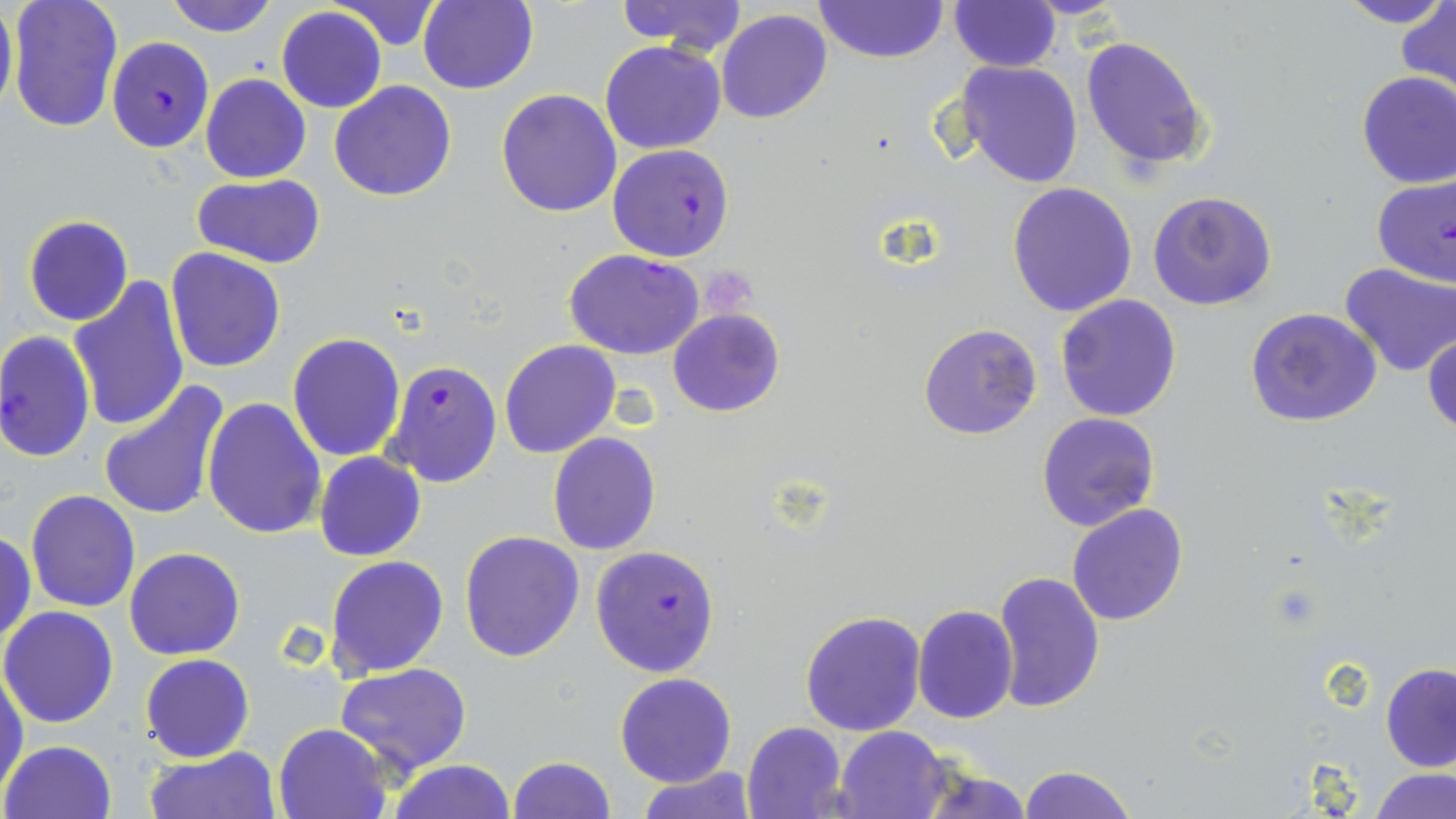
slide-level diagnosis = Plasmodium falciparum
magnification = 1000x
image size = 1456×819 pixels
field of view = single
preparation = thin blood smear
platelet locations = approximate bounding boxes as named x1/y1/x2/y2 corners in pixels: (x1=701, y1=271, x2=757, y2=321)
uninfected red blood cell locations = approximate bounding boxes as named x1/y1/x2/y2 corners in pixels: (x1=0, y1=0, x2=16, y2=121), (x1=5, y1=0, x2=123, y2=134), (x1=164, y1=0, x2=280, y2=37), (x1=612, y1=0, x2=748, y2=56), (x1=1333, y1=0, x2=1453, y2=30), (x1=325, y1=1, x2=446, y2=49), (x1=420, y1=1, x2=539, y2=95), (x1=814, y1=1, x2=949, y2=65), (x1=948, y1=1, x2=1060, y2=72), (x1=1399, y1=3, x2=1456, y2=93), (x1=277, y1=7, x2=386, y2=112), (x1=716, y1=10, x2=833, y2=124), (x1=1080, y1=35, x2=1211, y2=172), (x1=600, y1=41, x2=727, y2=153), (x1=956, y1=60, x2=1083, y2=187), (x1=1355, y1=72, x2=1456, y2=188), (x1=201, y1=74, x2=310, y2=183), (x1=330, y1=81, x2=457, y2=201), (x1=496, y1=89, x2=622, y2=216), (x1=191, y1=174, x2=328, y2=270), (x1=1007, y1=182, x2=1138, y2=318), (x1=1147, y1=190, x2=1277, y2=311), (x1=22, y1=214, x2=134, y2=326), (x1=166, y1=247, x2=285, y2=373), (x1=1339, y1=263, x2=1455, y2=378), (x1=68, y1=276, x2=190, y2=433), (x1=1055, y1=295, x2=1183, y2=423), (x1=1244, y1=307, x2=1384, y2=428), (x1=667, y1=309, x2=784, y2=418), (x1=917, y1=322, x2=1043, y2=442), (x1=1424, y1=329, x2=1456, y2=438), (x1=287, y1=333, x2=407, y2=462), (x1=500, y1=340, x2=619, y2=458), (x1=98, y1=379, x2=231, y2=524), (x1=203, y1=398, x2=326, y2=541), (x1=1036, y1=413, x2=1159, y2=531), (x1=547, y1=432, x2=661, y2=555), (x1=314, y1=452, x2=425, y2=561), (x1=26, y1=489, x2=140, y2=612), (x1=1067, y1=503, x2=1188, y2=625), (x1=1, y1=528, x2=36, y2=650), (x1=459, y1=530, x2=585, y2=661), (x1=124, y1=548, x2=245, y2=660), (x1=325, y1=555, x2=450, y2=678), (x1=990, y1=570, x2=1106, y2=712), (x1=912, y1=604, x2=1018, y2=723), (x1=0, y1=606, x2=119, y2=728), (x1=800, y1=610, x2=928, y2=737), (x1=140, y1=653, x2=253, y2=762), (x1=336, y1=662, x2=473, y2=775), (x1=1381, y1=662, x2=1456, y2=770), (x1=0, y1=665, x2=27, y2=797), (x1=614, y1=673, x2=738, y2=787), (x1=274, y1=721, x2=392, y2=818), (x1=741, y1=721, x2=847, y2=819), (x1=833, y1=727, x2=950, y2=818), (x1=2, y1=739, x2=116, y2=818), (x1=145, y1=746, x2=280, y2=819), (x1=507, y1=755, x2=615, y2=819), (x1=386, y1=758, x2=516, y2=819), (x1=911, y1=761, x2=1033, y2=817), (x1=1016, y1=764, x2=1139, y2=819), (x1=638, y1=766, x2=759, y2=819), (x1=1373, y1=767, x2=1455, y2=818)
modality = light microscopy
stain = May-Grünwald-Giemsa
Plasmodium falciparum-infected red blood cell locations = approximate bounding boxes as named x1/y1/x2/y2 corners in pixels: (x1=106, y1=36, x2=214, y2=152), (x1=608, y1=143, x2=734, y2=263), (x1=1372, y1=176, x2=1455, y2=288), (x1=565, y1=248, x2=704, y2=360), (x1=0, y1=331, x2=95, y2=463), (x1=382, y1=358, x2=502, y2=488), (x1=590, y1=544, x2=720, y2=677)